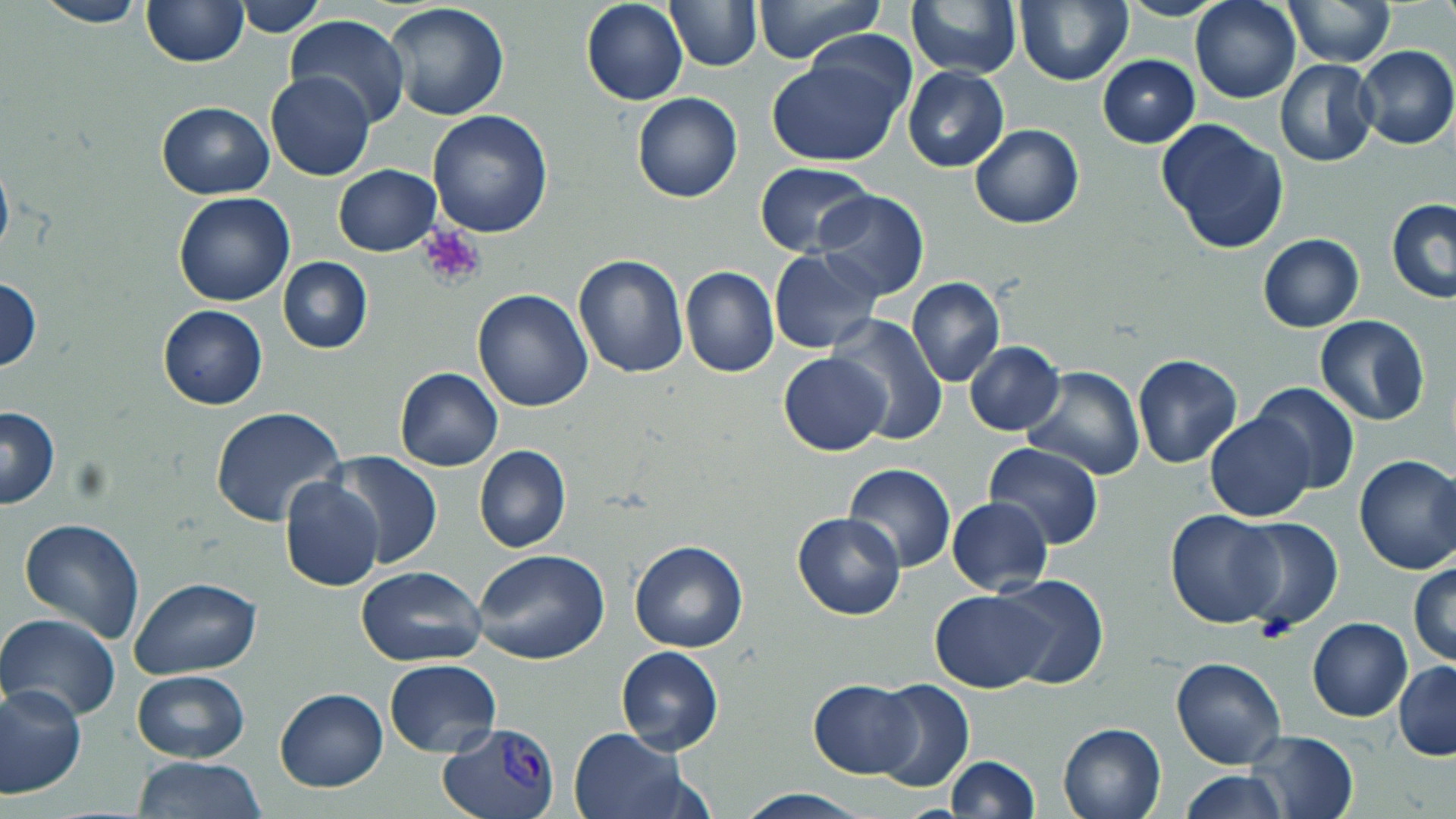

slide_level_diagnosis: Plasmodium vivax
preparation: thin blood smear
image_size: 1456×819 pixels
plasmodium_vivax_infected_red_blood_cell_locations: 'approximate bounding boxes as (x1, y1, x2, y2) in pixels: (438, 720, 560, 819)'
modality: light microscopy
stain: May-Grünwald-Giemsa
uninfected_red_blood_cell_locations: 'approximate bounding boxes as (x1, y1, x2, y2) in pixels: (233, 0, 326, 37), (581, 0, 687, 105), (666, 0, 761, 70), (753, 0, 883, 64), (905, 0, 1020, 80), (1190, 0, 1300, 103), (34, 1, 150, 27), (141, 1, 248, 67), (1284, 1, 1394, 68), (1013, 2, 1133, 86), (384, 3, 510, 120), (285, 14, 409, 128), (1355, 45, 1456, 151), (764, 47, 912, 168), (1097, 54, 1200, 147), (1275, 59, 1378, 166), (902, 67, 1009, 173), (266, 72, 375, 182), (631, 92, 742, 204), (155, 101, 275, 199), (427, 110, 553, 238), (1155, 116, 1290, 254), (970, 125, 1083, 229), (0, 149, 14, 270), (332, 164, 440, 256), (755, 164, 875, 258), (816, 189, 930, 302), (173, 192, 294, 307), (1386, 199, 1456, 304), (1258, 233, 1364, 331), (768, 248, 881, 353), (573, 254, 688, 376), (277, 257, 372, 354), (680, 265, 779, 378), (1, 275, 41, 372), (907, 277, 1006, 386), (472, 288, 595, 412), (158, 305, 268, 410), (828, 315, 948, 444), (1314, 315, 1430, 426), (964, 341, 1065, 436), (777, 353, 891, 456), (1131, 354, 1243, 468), (394, 367, 502, 471), (1022, 367, 1147, 480), (1250, 383, 1361, 494), (0, 405, 60, 511), (209, 406, 345, 530), (1205, 413, 1315, 522), (984, 442, 1105, 549), (474, 444, 570, 554), (326, 452, 445, 570), (1353, 454, 1456, 574), (1427, 462, 1456, 572), (843, 463, 957, 572), (280, 476, 384, 591), (946, 495, 1052, 597), (1165, 508, 1285, 629), (792, 511, 905, 620), (1232, 516, 1344, 633), (19, 518, 146, 642), (628, 538, 749, 653), (471, 549, 610, 666), (1408, 561, 1456, 667), (353, 564, 487, 667), (994, 573, 1109, 688), (130, 577, 261, 678), (930, 591, 1053, 691), (0, 612, 121, 722), (1307, 617, 1414, 723), (616, 645, 724, 754), (1171, 656, 1287, 770), (384, 658, 501, 756), (1395, 661, 1456, 761), (131, 670, 250, 762), (870, 678, 974, 792), (808, 679, 919, 778), (0, 684, 86, 798), (275, 687, 388, 793), (1058, 722, 1166, 818), (568, 728, 690, 819), (1245, 731, 1360, 819), (134, 756, 264, 818), (945, 756, 1038, 818), (1180, 769, 1288, 819), (735, 789, 871, 818)'
platelet_locations: 'approximate bounding boxes as (x1, y1, x2, y2) in pixels: (417, 225, 487, 290), (1252, 617, 1296, 646)'
field_of_view: one of a larger specimen
magnification: 1000x